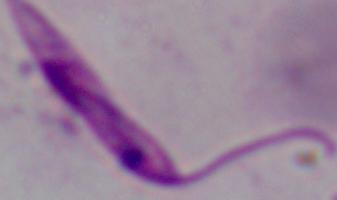
1000x magnification. A Leishmania parasite is shown. Photomicrograph.